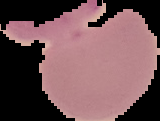
The area outside the segmented cell region is set to black. From a thin blood film. Image is 160×121 pixels. Malaria status: uninfected.